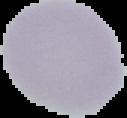
image_size: 127×118 pixels
image_type: cell region segmented out of the field of view; surrounding area masked to black
result: no Plasmodium parasites detected
preparation: thin blood smear